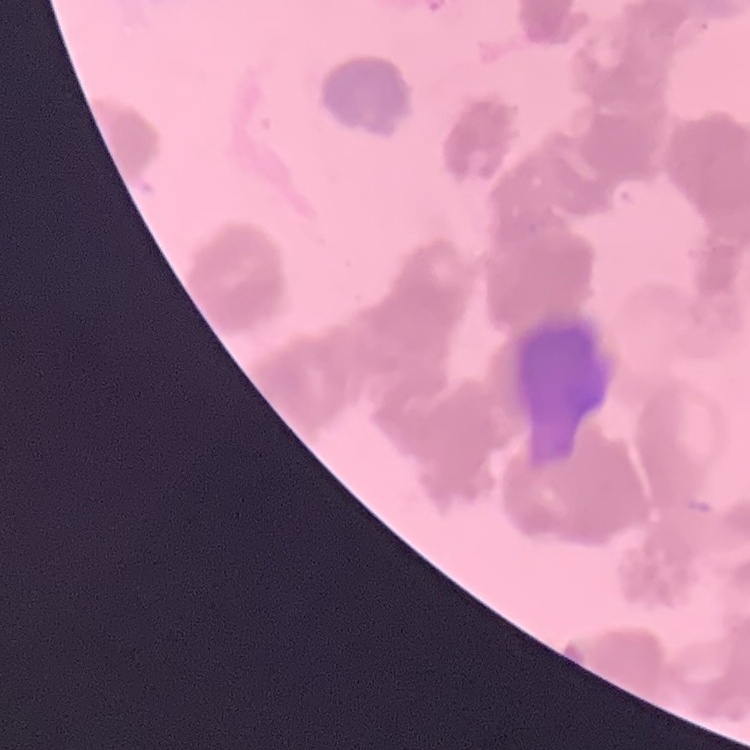

The erythrocytes exhibit rouleaux formation. Thin peripheral smear. Field's or Giemsa stain. One tile cut from a larger photomicrograph.